Outline platelets.
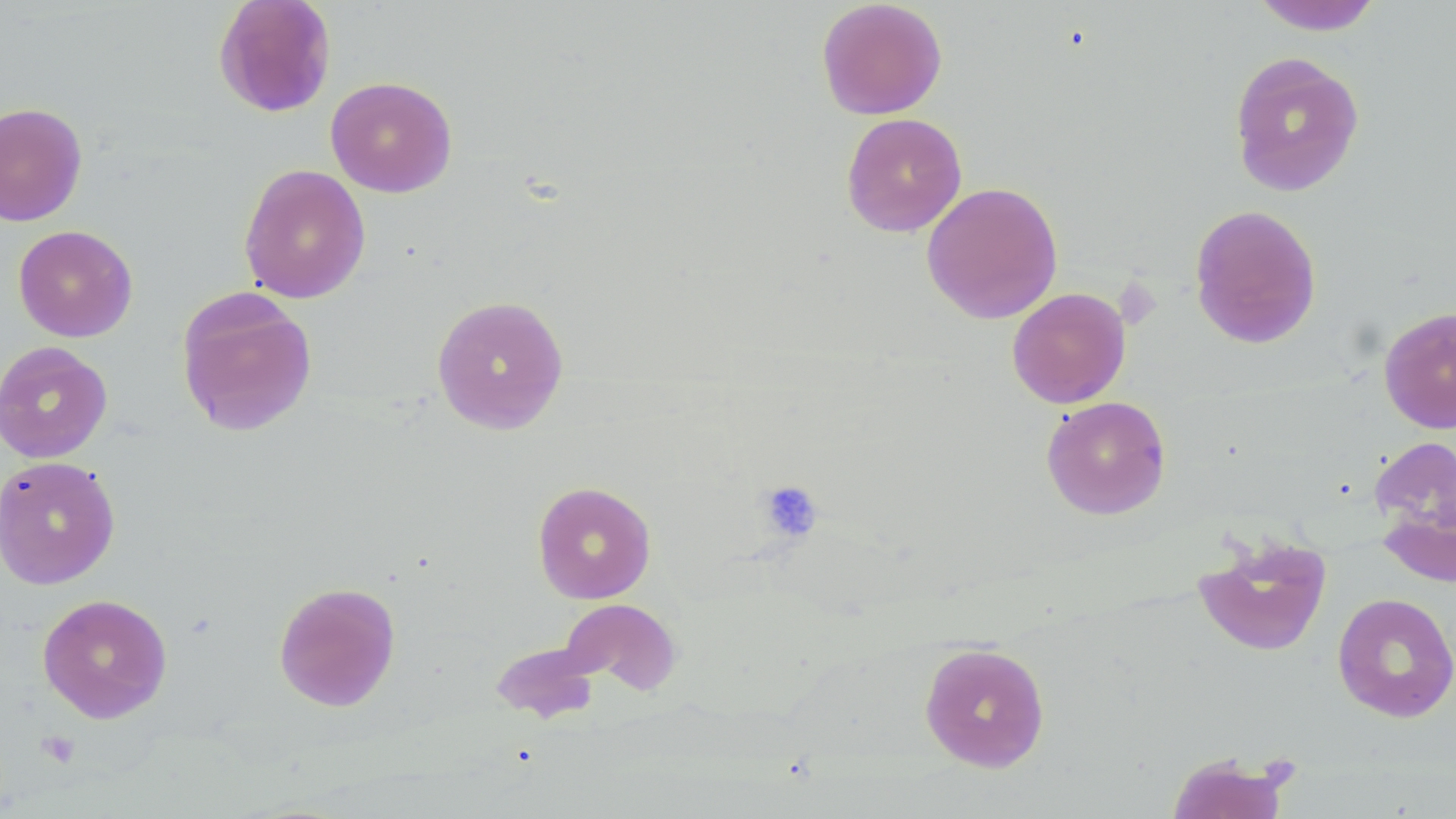

Approximate bounding boxes as (x1,y1)-(x2,y2) corner pairs in pixels.
Platelets: (757,480)-(824,543), (37,730)-(81,768).

slide-level diagnosis = no evidence of blood parasites
uninfected red blood cell locations = approximate bounding boxes as (x1,y1)-(x2,y2) corner pairs in pixels: (213,0)-(337,118), (816,0)-(947,120), (1249,0)-(1384,35), (1228,51)-(1365,197), (325,76)-(457,198), (0,101)-(88,227), (841,112)-(967,237), (239,163)-(371,304), (921,181)-(1063,324), (1188,204)-(1323,350), (13,225)-(138,343), (176,287)-(318,438), (1006,287)-(1131,408), (431,294)-(569,435), (1378,306)-(1456,434), (0,341)-(113,463), (1041,396)-(1172,520), (1369,434)-(1456,567), (0,455)-(121,589), (532,481)-(657,604), (1193,533)-(1332,656), (273,581)-(401,712), (1332,592)-(1456,723), (37,593)-(173,723), (554,597)-(683,699), (918,642)-(1051,772), (1166,752)-(1291,819)
modality = light microscopy
magnification = 1000x
image size = 1456×819 pixels
preparation = thin blood film
field of view = single
stain = May-Grünwald-Giemsa